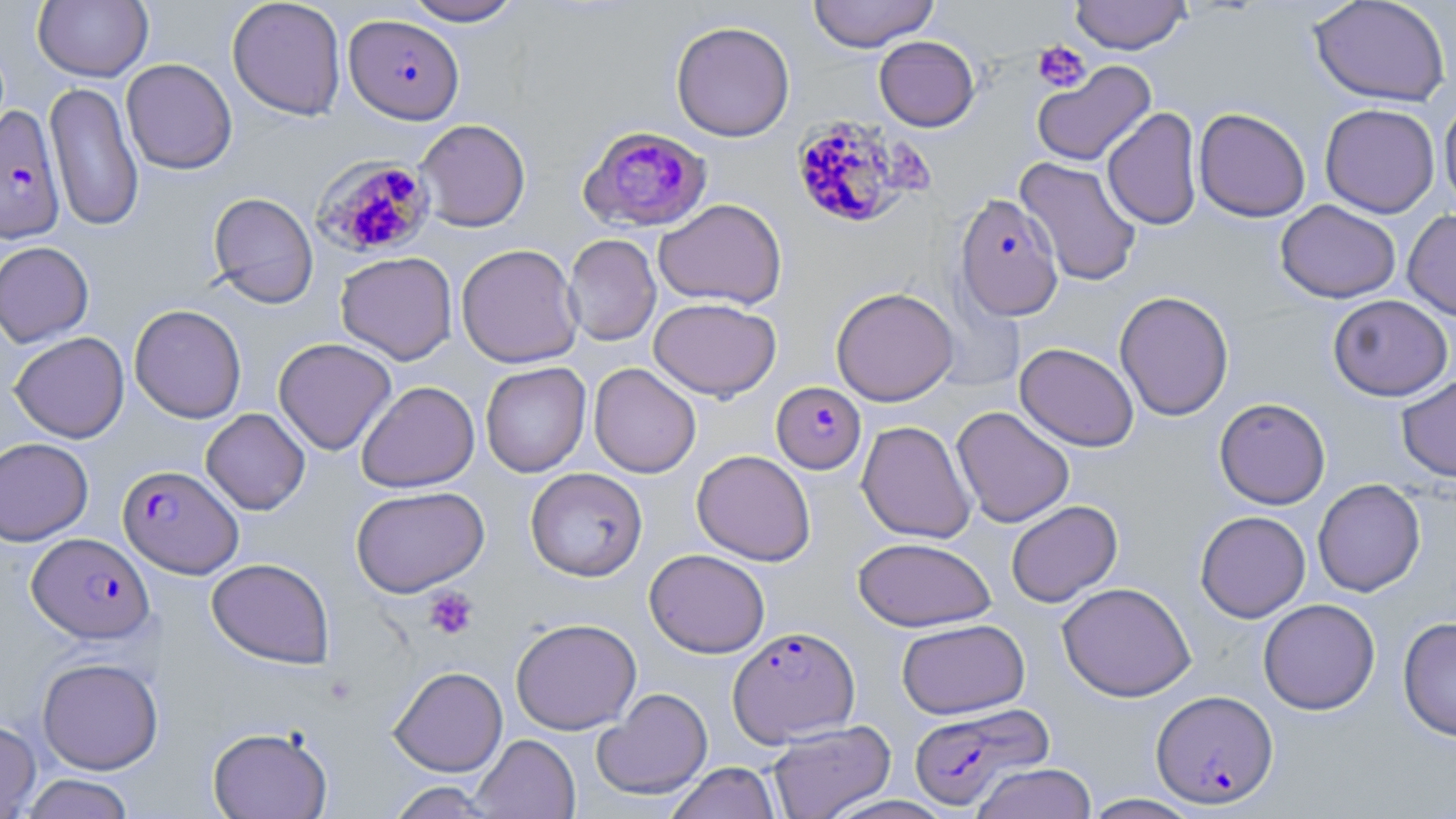
slide-level diagnosis = Plasmodium falciparum
field of view = single
uninfected red blood cell locations = approximate bounding boxes as (x1, y1, x2, y2) in pixels: (33, 0, 153, 82), (227, 0, 346, 120), (402, 0, 523, 26), (807, 0, 940, 52), (1069, 0, 1191, 54), (1309, 0, 1451, 106), (670, 20, 795, 142), (874, 36, 980, 131), (121, 58, 237, 175), (1032, 60, 1156, 167), (44, 81, 144, 232), (1438, 97, 1456, 212), (1320, 103, 1440, 218), (1102, 107, 1202, 230), (1194, 107, 1311, 222), (414, 118, 531, 232), (1015, 156, 1143, 287), (208, 191, 319, 308), (653, 198, 787, 309), (1275, 199, 1401, 303), (1403, 209, 1456, 321), (564, 234, 661, 346), (0, 241, 94, 347), (456, 243, 582, 368), (335, 252, 457, 365), (831, 287, 958, 406), (1114, 290, 1234, 421), (1327, 294, 1453, 401), (648, 297, 781, 401), (130, 304, 247, 423), (9, 331, 130, 443), (273, 338, 397, 455), (1015, 342, 1139, 452), (480, 362, 591, 477), (589, 363, 701, 478), (1396, 374, 1456, 482), (356, 381, 480, 492), (1214, 397, 1331, 509), (951, 406, 1075, 528), (201, 408, 310, 515), (856, 420, 976, 544), (0, 438, 93, 546), (691, 449, 815, 566), (525, 467, 648, 581), (1312, 478, 1425, 597), (350, 486, 489, 597), (1006, 500, 1123, 607), (1195, 510, 1311, 622), (853, 536, 997, 632), (644, 549, 770, 658), (206, 558, 334, 669), (1057, 582, 1195, 702), (1258, 599, 1380, 715), (1398, 616, 1456, 741), (510, 618, 641, 734), (896, 618, 1030, 719), (37, 657, 163, 774), (388, 666, 508, 776), (593, 688, 713, 800), (0, 719, 41, 818), (766, 720, 896, 819), (207, 725, 332, 819), (471, 734, 580, 819), (665, 762, 780, 819), (970, 762, 1097, 819), (19, 774, 136, 819), (386, 781, 500, 818), (1081, 794, 1204, 818)
preparation = thin blood smear
Plasmodium falciparum-infected red blood cell locations = approximate bounding boxes as (x1, y1, x2, y2) in pixels: (344, 14, 464, 124), (0, 106, 66, 244), (790, 114, 921, 230), (578, 125, 712, 232), (313, 155, 436, 259), (954, 193, 1064, 321), (771, 381, 866, 474), (118, 465, 243, 578), (28, 532, 154, 643), (727, 626, 860, 746), (1151, 690, 1278, 808), (908, 702, 1052, 810)
stain = May-Grünwald-Giemsa
modality = optical microscopy
image size = 1456×819 pixels
platelet locations = approximate bounding boxes as (x1, y1, x2, y2) in pixels: (1033, 40, 1091, 92), (424, 587, 478, 640)
magnification = 1000x